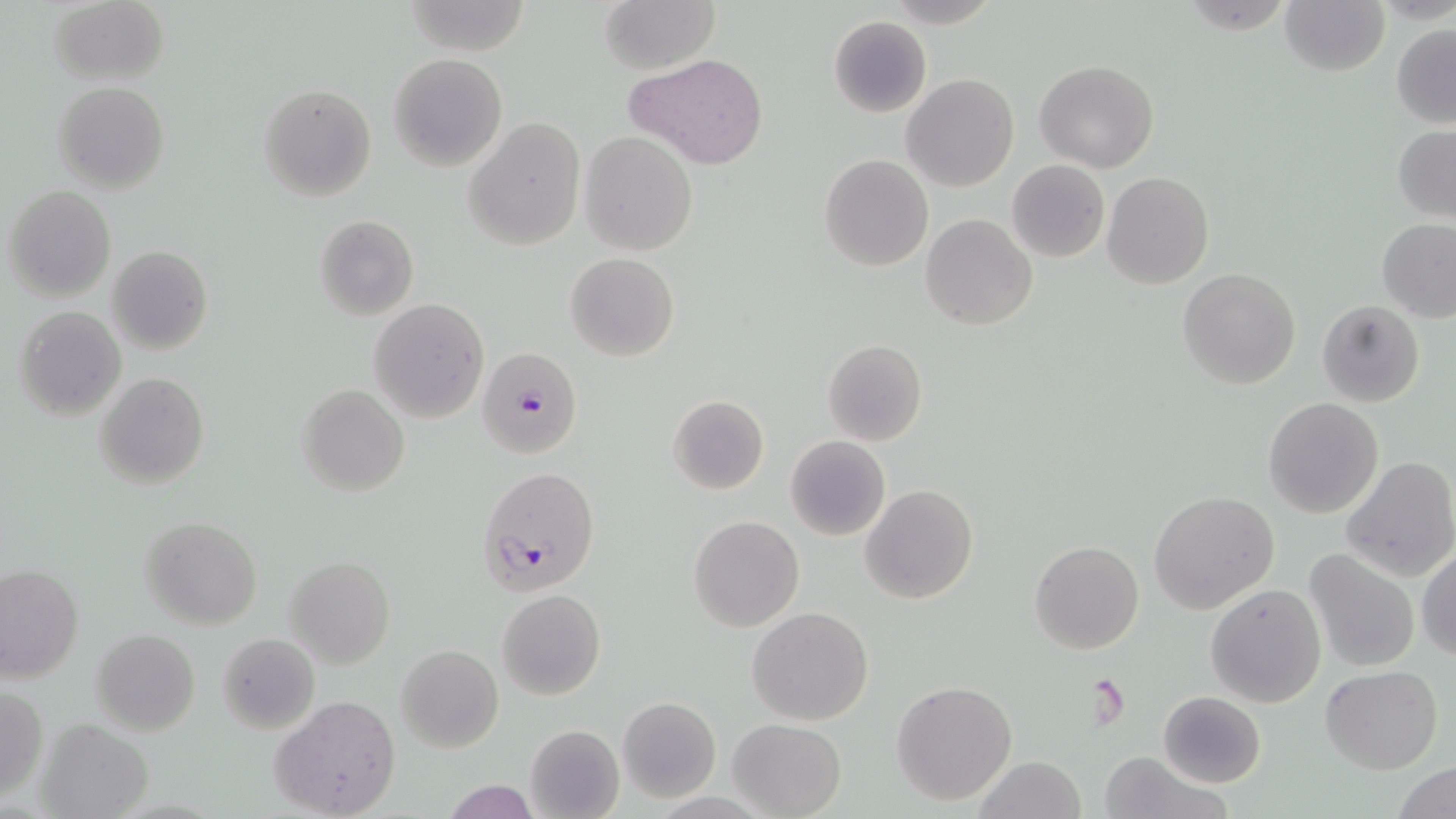
slide-level diagnosis = Plasmodium falciparum
image size = 1456×819 pixels
modality = light microscopy
stain = May-Grünwald-Giemsa
preparation = thin blood smear
Plasmodium falciparum-infected red blood cell locations = approximate bounding boxes as named x1/y1/x2/y2 corners in pixels: (x1=477, y1=347, x2=583, y2=460), (x1=475, y1=465, x2=600, y2=594)
uninfected red blood cell locations = approximate bounding boxes as named x1/y1/x2/y2 corners in pixels: (x1=49, y1=0, x2=170, y2=86), (x1=598, y1=0, x2=721, y2=74), (x1=1281, y1=0, x2=1389, y2=77), (x1=829, y1=15, x2=932, y2=117), (x1=1390, y1=24, x2=1456, y2=128), (x1=388, y1=53, x2=506, y2=171), (x1=628, y1=54, x2=769, y2=171), (x1=1035, y1=60, x2=1160, y2=173), (x1=901, y1=74, x2=1019, y2=191), (x1=52, y1=81, x2=170, y2=194), (x1=257, y1=83, x2=377, y2=202), (x1=463, y1=116, x2=586, y2=251), (x1=1392, y1=124, x2=1456, y2=224), (x1=580, y1=131, x2=698, y2=255), (x1=819, y1=153, x2=934, y2=271), (x1=1007, y1=160, x2=1109, y2=262), (x1=1102, y1=172, x2=1215, y2=291), (x1=5, y1=185, x2=116, y2=301), (x1=920, y1=213, x2=1037, y2=330), (x1=314, y1=214, x2=418, y2=321), (x1=1375, y1=218, x2=1456, y2=323), (x1=106, y1=246, x2=213, y2=355), (x1=565, y1=252, x2=680, y2=361), (x1=1178, y1=267, x2=1301, y2=390), (x1=368, y1=298, x2=489, y2=423), (x1=1316, y1=300, x2=1425, y2=407), (x1=13, y1=306, x2=126, y2=421), (x1=822, y1=339, x2=927, y2=446), (x1=96, y1=373, x2=209, y2=491), (x1=297, y1=384, x2=410, y2=496), (x1=667, y1=395, x2=769, y2=495), (x1=1263, y1=397, x2=1384, y2=519), (x1=786, y1=435, x2=890, y2=541), (x1=1341, y1=456, x2=1456, y2=582), (x1=860, y1=484, x2=979, y2=603), (x1=1148, y1=490, x2=1279, y2=614), (x1=688, y1=515, x2=805, y2=632), (x1=138, y1=516, x2=262, y2=629), (x1=1029, y1=539, x2=1144, y2=654), (x1=1416, y1=543, x2=1456, y2=662), (x1=1302, y1=549, x2=1419, y2=673), (x1=283, y1=556, x2=395, y2=670), (x1=1, y1=565, x2=83, y2=682), (x1=1206, y1=583, x2=1327, y2=707), (x1=497, y1=589, x2=605, y2=700), (x1=746, y1=607, x2=875, y2=727), (x1=90, y1=628, x2=201, y2=736), (x1=219, y1=634, x2=319, y2=733), (x1=396, y1=644, x2=503, y2=753), (x1=1320, y1=664, x2=1443, y2=774), (x1=892, y1=681, x2=1017, y2=805), (x1=0, y1=686, x2=47, y2=803), (x1=1157, y1=691, x2=1267, y2=789), (x1=270, y1=694, x2=401, y2=819), (x1=616, y1=697, x2=721, y2=802), (x1=36, y1=717, x2=154, y2=819), (x1=728, y1=719, x2=846, y2=818), (x1=523, y1=723, x2=624, y2=819), (x1=1098, y1=751, x2=1222, y2=819), (x1=973, y1=756, x2=1089, y2=818), (x1=1391, y1=762, x2=1456, y2=819), (x1=440, y1=780, x2=542, y2=818)
magnification = 1000x
field of view = one of a larger specimen